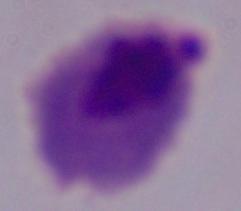

{
  "magnification": "1000x",
  "modality": "micrograph",
  "identification": "trichomonad"
}